Classify this cell by malaria status.
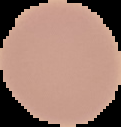
It is uninfected.

Image is 121×127 pixels. The area outside the segmented cell region is set to black. From a thin blood smear.